Assess this cell for malaria.
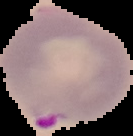

It is parasitized.

Summary:
  - Image size: 133×136 pixels
  - Image type: cell region segmented out of the field of view; surrounding area masked to black
  - Preparation: thin blood smear